Assess this cell for malaria.
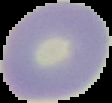

It is uninfected.

image_type: cell region segmented out of the field of view; surrounding area masked to black
preparation: thin blood film
image_size: 112×103 pixels